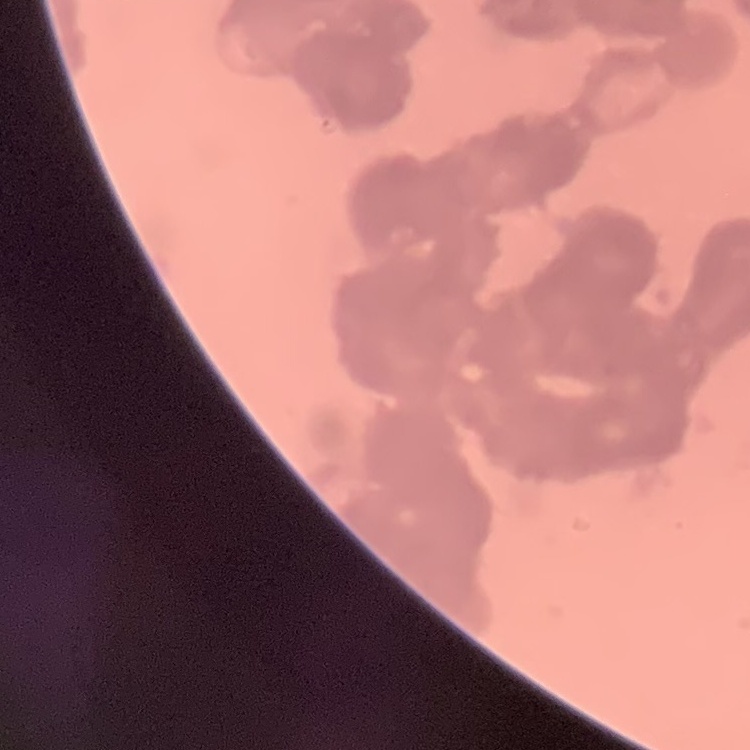

red blood cell morphology = rouleaux formation
preparation = thin peripheral smear
stain = Field's or Giemsa
image type = one tile cut from a larger photomicrograph